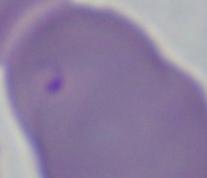

modality = micrograph
identification = Babesia
magnification = 1000x